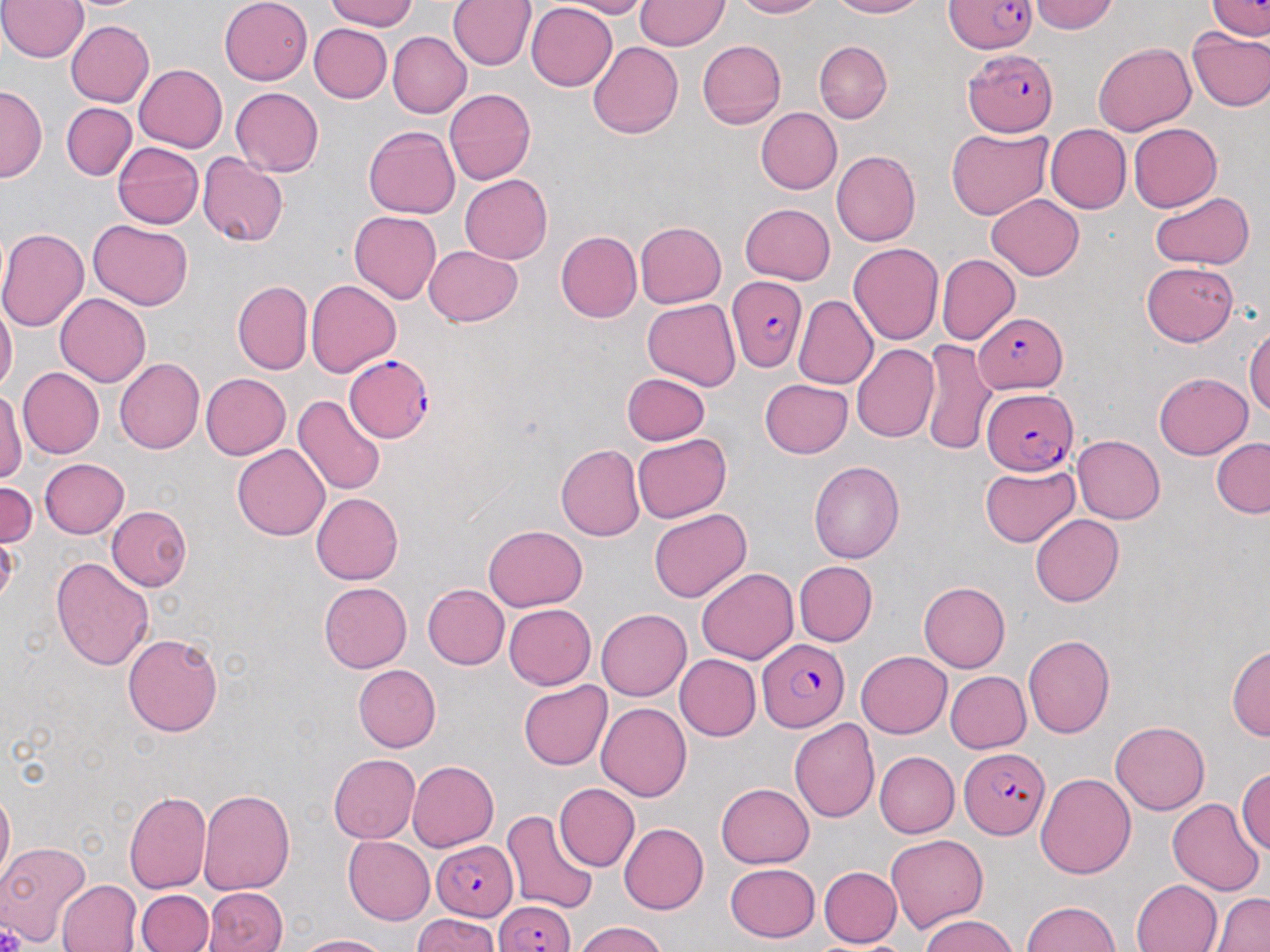
Approximate bounding boxes as named x1/y1/x2/y2 corners in pixels. Plasmodium falciparum-infected red blood cell locations: (x1=941, y1=0, x2=1038, y2=53), (x1=963, y1=49, x2=1056, y2=137), (x1=726, y1=278, x2=808, y2=371), (x1=977, y1=310, x2=1066, y2=396), (x1=345, y1=355, x2=433, y2=440), (x1=981, y1=387, x2=1076, y2=473), (x1=755, y1=639, x2=850, y2=733), (x1=963, y1=747, x2=1052, y2=839), (x1=431, y1=839, x2=518, y2=916), (x1=496, y1=893, x2=575, y2=952). Uninfected red blood cell locations: (x1=0, y1=0, x2=88, y2=63), (x1=217, y1=0, x2=310, y2=85), (x1=325, y1=0, x2=424, y2=30), (x1=448, y1=0, x2=534, y2=69), (x1=566, y1=0, x2=654, y2=16), (x1=636, y1=0, x2=728, y2=50), (x1=729, y1=0, x2=826, y2=19), (x1=828, y1=0, x2=933, y2=19), (x1=1032, y1=0, x2=1120, y2=34), (x1=1205, y1=0, x2=1269, y2=41), (x1=525, y1=5, x2=618, y2=89), (x1=65, y1=21, x2=155, y2=107), (x1=311, y1=25, x2=392, y2=105), (x1=1187, y1=27, x2=1270, y2=112), (x1=389, y1=31, x2=471, y2=117), (x1=1102, y1=37, x2=1270, y2=123), (x1=695, y1=40, x2=784, y2=129), (x1=588, y1=41, x2=687, y2=139), (x1=816, y1=42, x2=891, y2=124), (x1=1092, y1=43, x2=1195, y2=136), (x1=134, y1=63, x2=229, y2=153), (x1=1, y1=88, x2=43, y2=180), (x1=232, y1=88, x2=324, y2=176), (x1=444, y1=88, x2=536, y2=185), (x1=62, y1=102, x2=136, y2=180), (x1=755, y1=107, x2=842, y2=194), (x1=1127, y1=122, x2=1222, y2=212), (x1=1043, y1=123, x2=1131, y2=214), (x1=364, y1=126, x2=459, y2=217), (x1=946, y1=127, x2=1054, y2=219), (x1=111, y1=140, x2=206, y2=230), (x1=832, y1=151, x2=921, y2=244), (x1=198, y1=153, x2=289, y2=247), (x1=459, y1=175, x2=553, y2=264), (x1=1150, y1=191, x2=1253, y2=268), (x1=987, y1=196, x2=1084, y2=280), (x1=740, y1=202, x2=836, y2=282), (x1=349, y1=211, x2=441, y2=303), (x1=89, y1=219, x2=193, y2=310), (x1=634, y1=222, x2=726, y2=308), (x1=0, y1=228, x2=88, y2=336), (x1=556, y1=231, x2=642, y2=323), (x1=849, y1=240, x2=944, y2=349), (x1=426, y1=244, x2=524, y2=329), (x1=937, y1=254, x2=1019, y2=345), (x1=1141, y1=263, x2=1241, y2=346), (x1=306, y1=280, x2=401, y2=379), (x1=233, y1=281, x2=311, y2=373), (x1=55, y1=294, x2=150, y2=387), (x1=794, y1=296, x2=875, y2=392), (x1=642, y1=301, x2=740, y2=390), (x1=0, y1=305, x2=16, y2=398), (x1=1244, y1=320, x2=1270, y2=427), (x1=921, y1=339, x2=993, y2=454), (x1=852, y1=342, x2=938, y2=443), (x1=116, y1=357, x2=209, y2=454), (x1=16, y1=368, x2=103, y2=458), (x1=1154, y1=370, x2=1253, y2=458), (x1=621, y1=372, x2=712, y2=445), (x1=200, y1=373, x2=291, y2=460), (x1=759, y1=377, x2=853, y2=457), (x1=1, y1=387, x2=22, y2=491), (x1=291, y1=394, x2=386, y2=495), (x1=633, y1=433, x2=732, y2=522), (x1=1073, y1=435, x2=1165, y2=522), (x1=1211, y1=439, x2=1269, y2=517), (x1=231, y1=444, x2=329, y2=540), (x1=555, y1=444, x2=644, y2=540), (x1=41, y1=457, x2=129, y2=538), (x1=810, y1=460, x2=907, y2=562), (x1=981, y1=463, x2=1080, y2=548), (x1=0, y1=480, x2=39, y2=548), (x1=311, y1=491, x2=402, y2=585), (x1=108, y1=506, x2=192, y2=591), (x1=647, y1=509, x2=752, y2=602), (x1=1030, y1=514, x2=1124, y2=606), (x1=482, y1=525, x2=587, y2=611), (x1=51, y1=555, x2=154, y2=673), (x1=792, y1=560, x2=875, y2=646), (x1=696, y1=568, x2=798, y2=663), (x1=917, y1=580, x2=1009, y2=672), (x1=321, y1=581, x2=412, y2=672), (x1=424, y1=583, x2=509, y2=669), (x1=502, y1=604, x2=595, y2=689), (x1=597, y1=608, x2=691, y2=700), (x1=122, y1=633, x2=224, y2=737), (x1=1022, y1=634, x2=1117, y2=739), (x1=1229, y1=644, x2=1269, y2=747), (x1=857, y1=651, x2=952, y2=737), (x1=675, y1=655, x2=760, y2=740), (x1=354, y1=665, x2=441, y2=752), (x1=946, y1=671, x2=1030, y2=753), (x1=517, y1=681, x2=611, y2=771), (x1=595, y1=702, x2=691, y2=804), (x1=788, y1=715, x2=880, y2=827), (x1=1112, y1=719, x2=1212, y2=814), (x1=873, y1=751, x2=957, y2=839), (x1=328, y1=753, x2=421, y2=842), (x1=406, y1=761, x2=498, y2=852), (x1=1235, y1=766, x2=1270, y2=858), (x1=1036, y1=772, x2=1135, y2=878), (x1=716, y1=782, x2=816, y2=869), (x1=554, y1=783, x2=638, y2=871), (x1=197, y1=785, x2=297, y2=896), (x1=0, y1=788, x2=15, y2=887), (x1=122, y1=788, x2=211, y2=894), (x1=1169, y1=799, x2=1263, y2=895), (x1=504, y1=806, x2=597, y2=913), (x1=619, y1=823, x2=708, y2=915), (x1=886, y1=832, x2=990, y2=933), (x1=342, y1=836, x2=434, y2=925), (x1=2, y1=846, x2=107, y2=948), (x1=724, y1=863, x2=819, y2=943), (x1=819, y1=866, x2=901, y2=946), (x1=1132, y1=878, x2=1221, y2=952), (x1=59, y1=879, x2=140, y2=952), (x1=205, y1=887, x2=289, y2=952), (x1=137, y1=889, x2=214, y2=951), (x1=1214, y1=892, x2=1270, y2=952), (x1=1021, y1=900, x2=1121, y2=952), (x1=918, y1=912, x2=1019, y2=952), (x1=407, y1=914, x2=503, y2=952), (x1=572, y1=921, x2=672, y2=952), (x1=293, y1=933, x2=393, y2=951). Platelet locations: (x1=0, y1=539, x2=20, y2=594), (x1=0, y1=926, x2=27, y2=952). Slide-level diagnosis: Plasmodium falciparum. May-Grünwald-Giemsa stain. Captured at 1000x magnification. Light microscopy. Thin blood smear. Image is 1270×952 pixels. Single field of view.